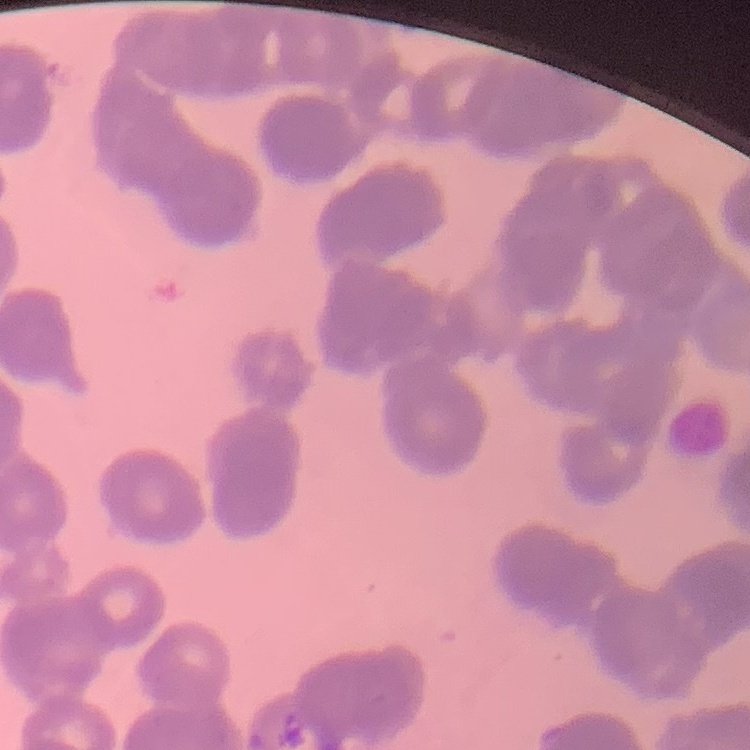

Summary:
  - Erythrocyte morphology: rouleaux formation
  - Preparation: thin blood smear
  - Stain: Field's or Giemsa
  - Image type: square crop of a larger photomicrograph